Report the malaria status of this cell.
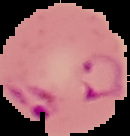

Parasitized.

{
  "preparation": "thin blood smear",
  "image_type": "segmented cell region on a black background",
  "image_size": "130×136 pixels"
}